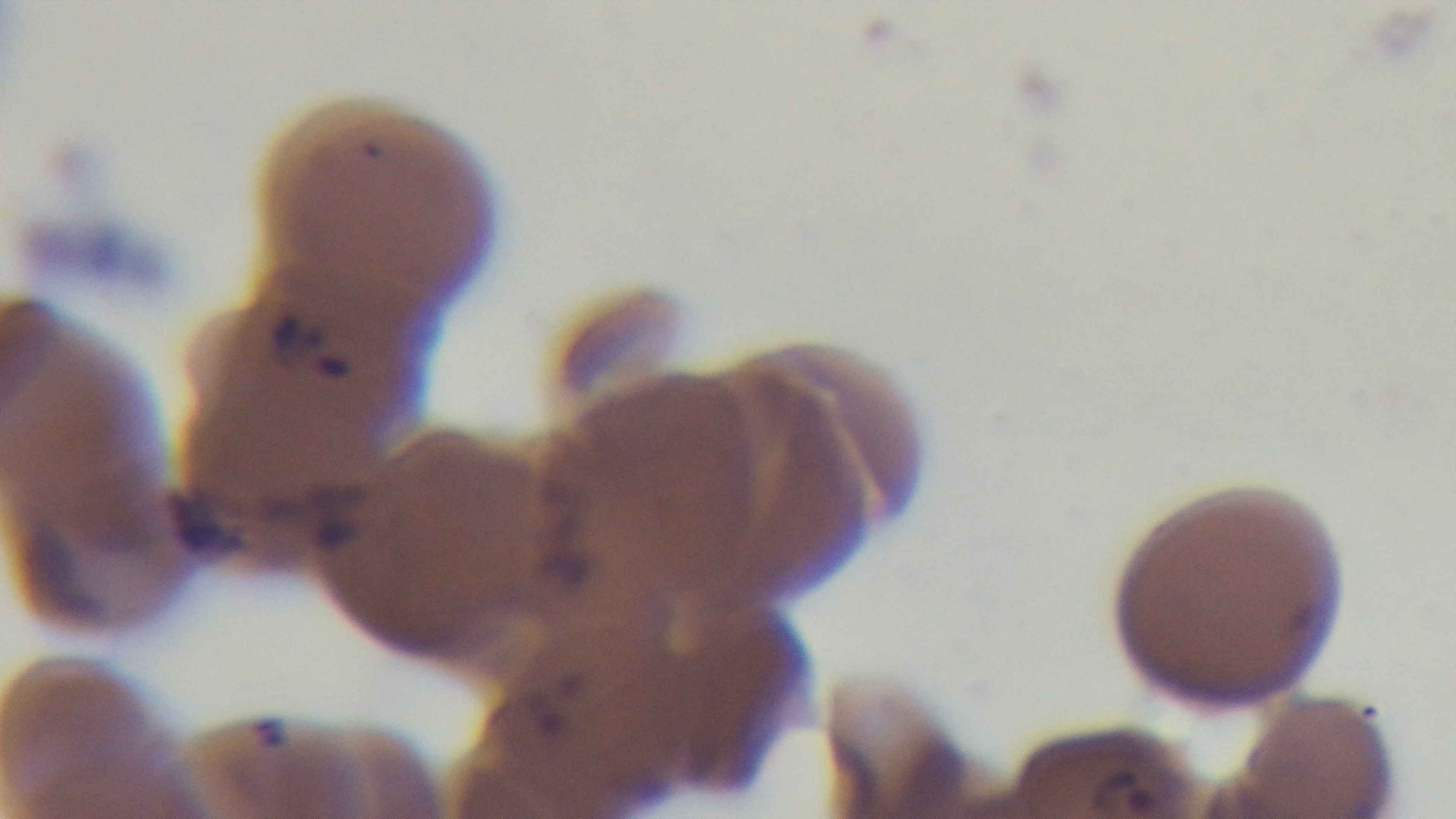
malaria status = infected
preparation = thin smear
field of view = one from the slide
stain = Giemsa
modality = light microscopy
capture = mounted 4K digital camera
objective = 100x oil immersion